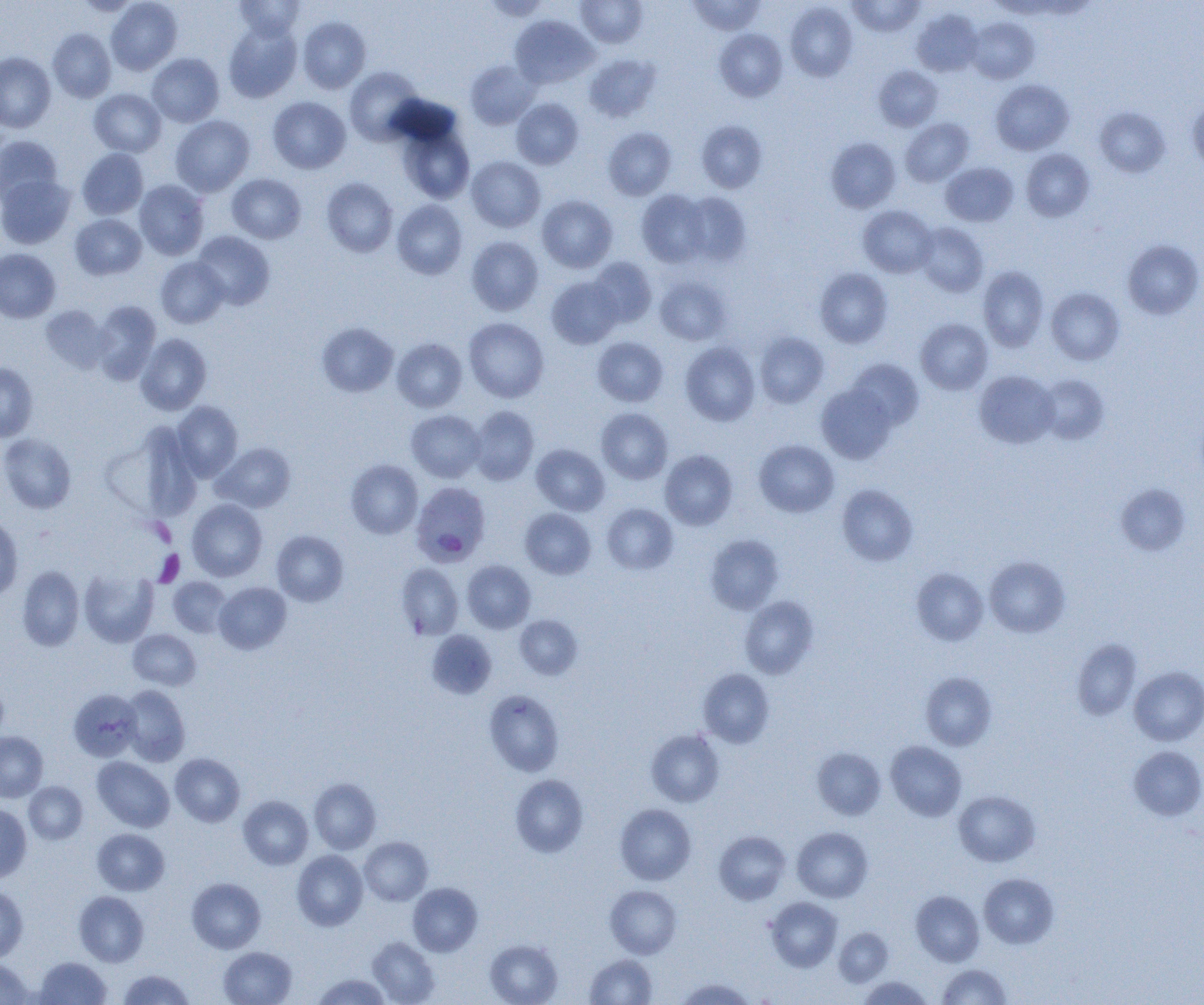

Approximate bounding boxes as (x1,y1)-(x2,y2) corner pairs in pixels. Plasmodium falciparum-infected red blood cell locations: (409,483)-(489,569). Uninfected red blood cell locations: (73,0)-(142,17), (106,0)-(182,75), (234,0)-(305,40), (576,0)-(648,47), (687,0)-(766,35), (847,0)-(926,36), (785,2)-(858,82), (911,8)-(983,77), (509,15)-(598,89), (297,16)-(371,94), (966,17)-(1039,84), (223,20)-(302,103), (48,28)-(116,102), (714,29)-(787,101), (0,52)-(56,132), (147,53)-(224,127), (584,53)-(661,122), (465,59)-(540,129), (873,65)-(943,131), (344,66)-(425,145), (990,79)-(1074,155), (89,89)-(166,157), (267,96)-(351,174), (511,98)-(583,170), (1187,98)-(1204,172), (1094,106)-(1170,177), (170,115)-(255,197), (901,118)-(973,186), (696,120)-(767,193), (397,124)-(475,204), (603,127)-(677,200), (0,136)-(63,205), (826,137)-(900,212), (77,148)-(148,220), (1021,149)-(1094,221), (467,156)-(545,232), (941,162)-(1018,226), (227,173)-(306,244), (0,174)-(76,249), (321,178)-(397,257), (134,180)-(209,260), (636,189)-(711,267), (681,192)-(752,266), (537,195)-(617,272), (391,200)-(467,279), (858,205)-(937,277), (70,214)-(146,280), (915,223)-(988,296), (192,231)-(275,310), (466,236)-(544,316), (1123,239)-(1204,320), (0,248)-(61,323), (155,257)-(228,328), (588,257)-(657,327), (978,266)-(1049,352), (814,267)-(893,348), (546,276)-(623,349), (655,276)-(732,345), (1046,287)-(1124,365), (90,301)-(161,384), (40,304)-(112,373), (464,317)-(549,402), (916,318)-(993,395), (317,322)-(398,397), (754,332)-(829,408), (135,333)-(212,415), (592,337)-(668,407), (391,338)-(467,412), (680,341)-(760,426), (846,359)-(924,430), (0,362)-(38,442), (974,370)-(1059,448), (1036,374)-(1109,445), (816,383)-(898,464), (172,401)-(243,481), (469,406)-(539,485), (596,408)-(673,484), (406,410)-(485,483), (105,422)-(203,522), (0,432)-(77,514), (754,440)-(839,517), (212,442)-(296,513), (531,444)-(609,516), (660,449)-(738,530), (346,460)-(423,539), (1115,483)-(1191,556), (836,485)-(918,566), (187,499)-(267,581), (602,503)-(679,574), (520,508)-(596,579), (0,516)-(23,602), (272,530)-(349,607), (705,533)-(785,614), (984,556)-(1070,637), (462,560)-(535,633), (396,562)-(463,640), (16,565)-(85,651), (911,567)-(988,646), (79,569)-(158,647), (168,577)-(232,637), (214,582)-(291,654), (739,595)-(819,678), (515,615)-(582,680), (128,630)-(201,691), (427,630)-(497,699), (1072,638)-(1141,720), (1129,666)-(1204,745), (698,668)-(774,747), (920,672)-(997,750), (0,676)-(9,743), (119,685)-(190,766), (68,689)-(142,762), (484,689)-(564,776), (647,729)-(725,807), (0,731)-(48,801), (886,741)-(966,821), (1128,745)-(1204,820), (812,747)-(886,819), (170,753)-(245,827), (92,756)-(174,832), (510,774)-(588,857), (309,778)-(381,854), (24,781)-(88,844), (953,790)-(1040,867), (238,796)-(313,870), (0,802)-(32,883), (614,803)-(696,885), (792,827)-(873,902), (92,828)-(170,896), (714,830)-(790,904), (359,836)-(433,905), (292,850)-(368,931), (979,873)-(1058,949), (187,878)-(266,953), (408,882)-(482,956), (605,885)-(682,958), (0,887)-(28,962), (911,890)-(984,966), (74,891)-(148,967), (765,897)-(842,971), (834,928)-(893,986), (367,937)-(440,1005), (485,938)-(563,1005), (219,947)-(296,1005), (585,954)-(657,1005), (35,956)-(111,1004), (0,958)-(34,1004), (937,964)-(1011,1005), (118,970)-(194,1004), (313,973)-(390,1005), (859,976)-(933,1004), (676,978)-(755,1004). Platelet locations: (155,550)-(185,586). Slide-level diagnosis: Plasmodium falciparum. Thin blood film. Optical microscopy. Single field of view. 1000x magnification. Image is 1204×1005 pixels.